Point out every malaria parasite and every leukocyte.
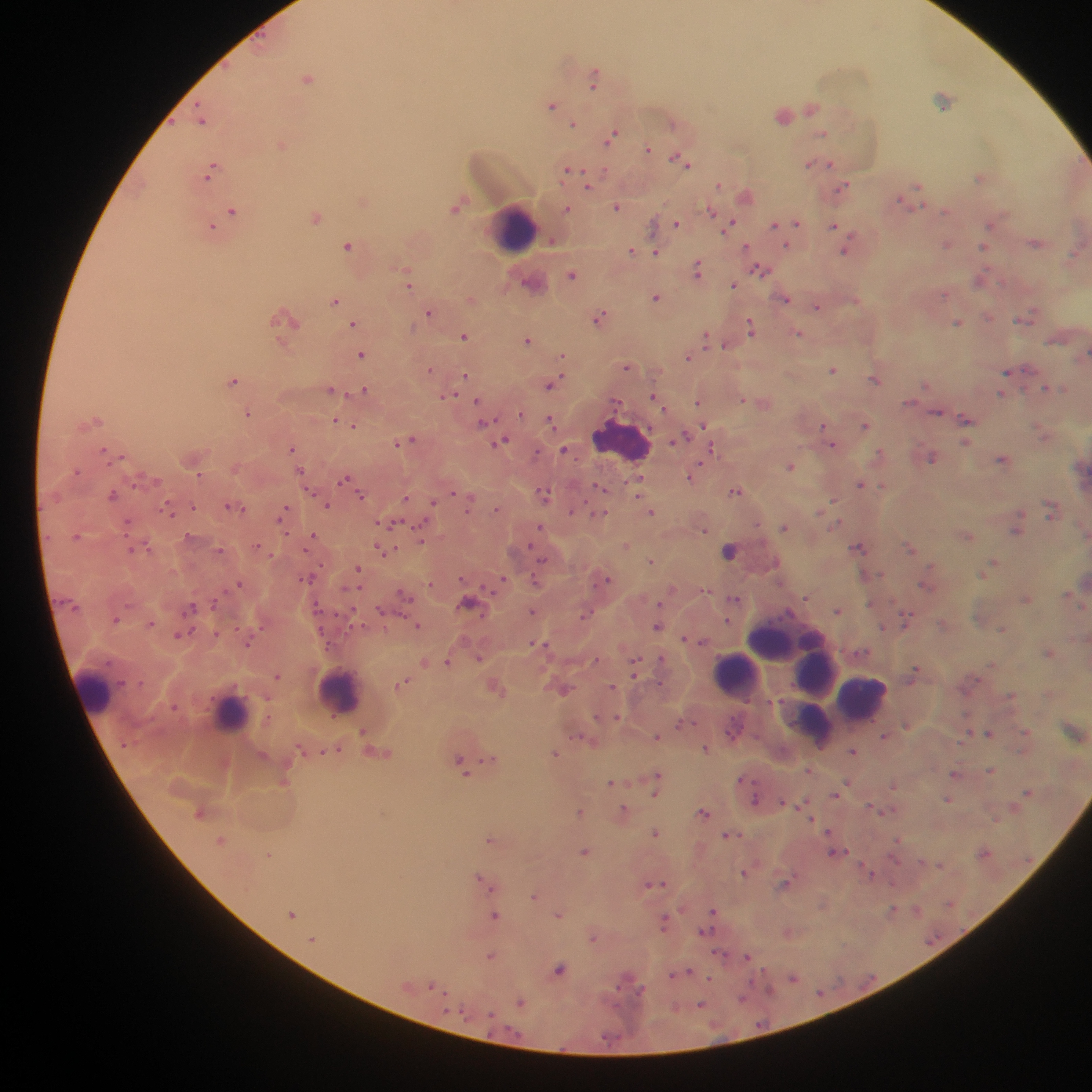

Approximate centers as x y in pixels.
Malaria parasites: 595 72; 197 102; 553 104; 813 108; 202 121; 574 123; 674 125; 823 133; 612 136; 281 145; 648 148; 677 156; 809 164; 831 164; 689 165; 567 169; 587 169; 605 169; 979 178; 718 184; 919 185; 843 186; 588 187; 618 207; 567 209; 232 210; 710 211; 946 211; 318 219; 732 222; 797 222; 676 223; 774 224; 835 225; 990 225; 852 236; 787 244; 348 245; 947 245; 985 245; 746 247; 845 250; 632 251; 657 253; 987 268; 406 269; 759 269; 698 274; 410 283; 734 285; 945 294; 657 297; 788 299; 336 303; 817 307; 429 313; 602 313; 989 317; 283 318; 599 319; 1021 321; 959 322; 354 323; 749 323; 751 332; 799 333; 465 337; 527 339; 707 343; 725 345; 362 354; 564 356; 688 358; 627 365; 431 370; 833 370; 1008 372; 466 376; 562 376; 874 378; 235 380; 555 383; 550 386; 1046 387; 365 389; 332 390; 347 393; 454 394; 652 396; 478 399; 743 400; 699 403; 663 408; 249 413; 521 415; 99 419; 551 420; 336 421; 487 422; 340 424; 704 425; 354 426; 865 426; 822 427; 686 435; 414 440; 504 440; 673 440; 397 443; 833 445; 712 446; 104 448; 292 448; 562 448; 878 451; 536 452; 120 457; 933 458; 1002 458; 701 462; 790 467; 301 470; 200 474; 344 479; 862 484; 881 485; 598 487; 734 492; 453 493; 544 493; 113 494; 314 494; 638 494; 361 495; 471 496; 405 498; 433 500; 835 500; 585 501; 1050 503; 167 504; 194 506; 227 506; 327 506; 286 508; 496 509; 242 510; 468 510; 571 510; 651 511; 822 511; 603 513; 173 514; 1022 514; 1051 514; 1050 515; 128 520; 279 521; 381 522; 398 523; 422 523; 757 524; 836 525; 540 526; 783 527; 704 530; 1018 530; 314 534; 288 535; 76 536; 126 537; 422 542; 257 546; 529 546; 378 548; 397 548; 858 548; 910 548; 148 549; 221 549; 305 550; 131 551; 730 552; 543 561; 651 562; 993 562; 323 563; 930 564; 359 567; 879 573; 504 577; 462 578; 535 578; 304 579; 607 580; 240 582; 430 583; 483 586; 359 588; 345 591; 706 591; 1069 593; 806 596; 409 598; 734 598; 214 602; 659 604; 870 604; 129 605; 191 606; 318 606; 353 610; 838 610; 381 611; 533 611; 401 614; 904 614; 482 615; 584 616; 728 619; 115 620; 152 623; 363 624; 419 625; 658 626; 882 626; 235 628; 1001 629; 260 630; 193 631; 321 631; 217 632; 177 635; 685 638; 703 642; 533 643; 538 644; 546 644; 249 645; 330 647; 660 658; 479 659; 596 659; 636 659; 424 662; 446 662; 917 668; 277 675; 633 677; 977 678; 141 681; 404 681; 660 684; 612 685; 1011 695; 266 699; 749 699; 175 705; 618 716; 966 716; 269 717; 595 717; 602 717; 1026 730; 362 731; 990 733; 578 735; 884 735; 657 737; 299 747; 705 749; 323 751; 852 751; 555 754; 459 757; 486 757; 809 770; 991 770; 658 772; 953 774; 739 780; 629 781; 754 782; 610 783; 893 787; 1027 792; 654 794; 836 796; 949 799; 755 800; 805 800; 782 801; 869 806; 624 807; 890 810; 580 811; 704 811; 810 819; 995 820; 828 830; 656 832; 739 834; 726 835; 898 839; 221 840; 491 840; 846 850; 584 851; 832 852; 270 854; 895 859; 939 864; 744 874; 872 874; 795 875; 480 876; 664 883; 892 883; 648 884; 786 885; 492 890; 534 896; 893 908; 897 908; 681 909; 714 910; 291 915; 495 915; 558 915; 665 917; 665 930; 705 931; 593 937; 719 951; 490 955; 747 957; 558 968; 689 971; 672 974; 794 977; 710 978; 753 980; 429 985; 618 987; 643 988; 821 991; 447 992; 448 998; 743 998; 522 1002; 701 1003; 446 1010; 490 1013.
Leukocytes: 515 226; 617 431; 783 636; 818 670; 731 673; 92 690; 342 695; 861 698; 226 708; 817 725.

image size = 1092×1092 pixels
field of view = single
capture = mobile-phone photograph through a microscope
country = Ghana
preparation = thick blood film